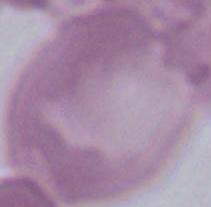
identification: red blood cell
modality: micrograph
magnification: 1000x